Classify this cell by malaria status.
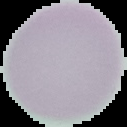
It is uninfected.

Image is 127×127 pixels. Segmented cell region on a black background. From a thin blood film.